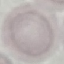

{
  "malaria_status": "uninfected",
  "stain": "Giemsa",
  "preparation": "thin blood smear",
  "capture": "smartphone camera at the microscope eyepiece",
  "image_type": "automatically extracted cell patch, resized to 64 × 64 pixels"
}